Name the blood parasite species.
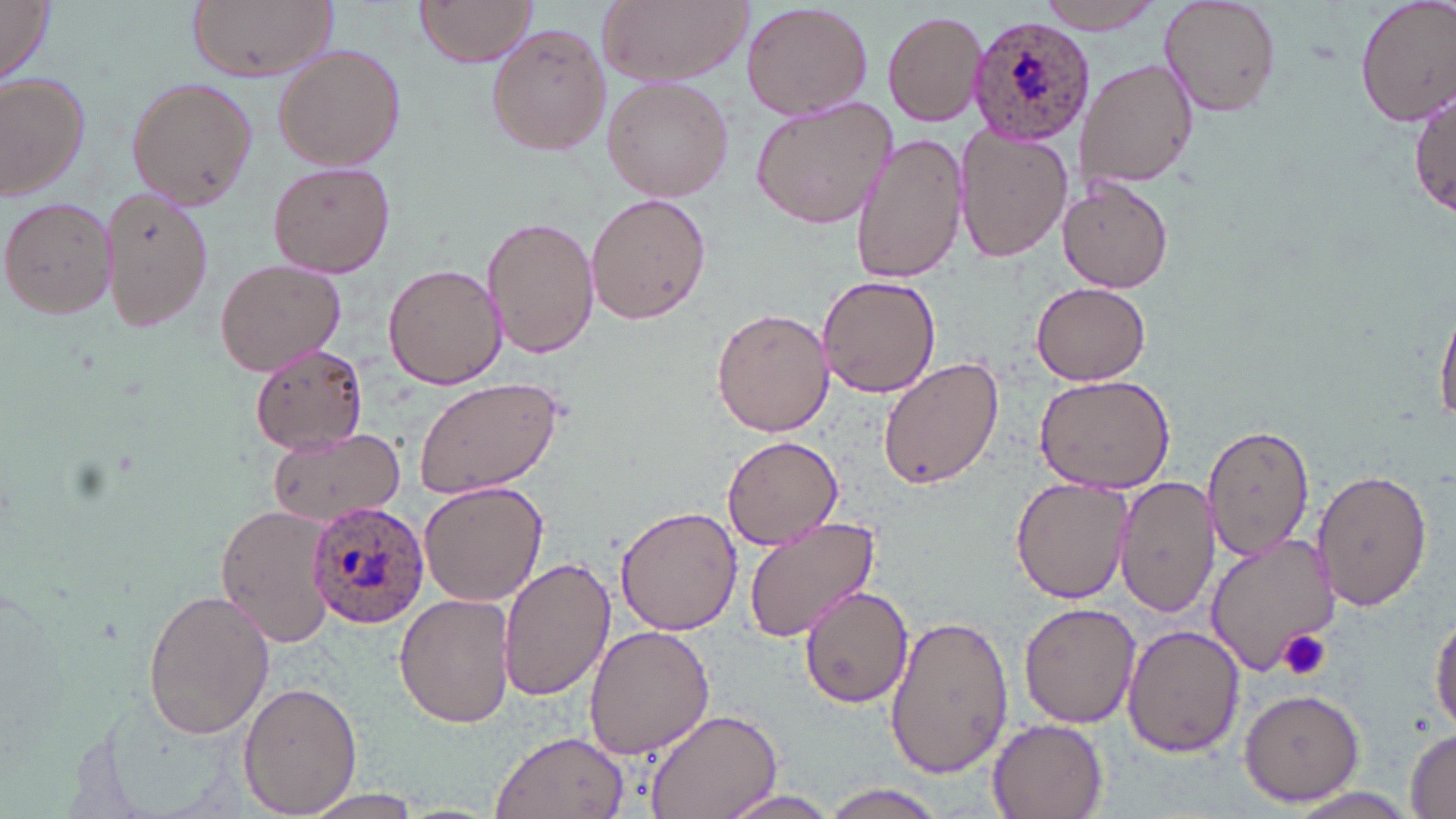

Plasmodium ovale.

Approximate bounding boxes as (x1, y1, x2, y2) in pixels. Uninfected red blood cell locations: (0, 0, 57, 85), (186, 0, 336, 80), (594, 0, 754, 86), (1042, 0, 1164, 33), (1159, 0, 1283, 118), (1354, 0, 1456, 128), (412, 1, 539, 68), (739, 1, 874, 122), (881, 9, 988, 125), (486, 24, 611, 156), (272, 43, 407, 173), (1077, 59, 1198, 188), (0, 73, 92, 199), (127, 76, 259, 209), (604, 76, 734, 202), (1412, 87, 1456, 220), (751, 98, 895, 230), (954, 124, 1072, 264), (849, 131, 967, 285), (268, 161, 396, 278), (1058, 177, 1174, 292), (101, 185, 216, 336), (585, 193, 711, 325), (0, 196, 116, 319), (483, 216, 599, 359), (217, 257, 348, 377), (384, 264, 506, 389), (816, 275, 941, 398), (1031, 281, 1151, 384), (1435, 304, 1456, 430), (711, 308, 835, 437), (248, 342, 367, 456), (877, 354, 1003, 490), (1035, 372, 1174, 493), (411, 376, 563, 500), (1203, 422, 1316, 563), (266, 427, 404, 526), (721, 434, 844, 549), (1313, 467, 1434, 612), (1115, 477, 1221, 621), (1011, 480, 1134, 603), (418, 481, 547, 605), (215, 504, 335, 648), (615, 505, 742, 636), (740, 514, 881, 643), (1205, 532, 1341, 675), (497, 558, 616, 700), (799, 586, 912, 709), (141, 588, 275, 742), (393, 593, 517, 728), (1019, 601, 1141, 727), (1430, 611, 1456, 736), (882, 612, 1014, 780), (582, 624, 717, 761), (1125, 624, 1246, 758), (235, 683, 362, 813), (1239, 688, 1366, 806), (644, 707, 783, 819), (988, 717, 1109, 819), (1404, 725, 1455, 819), (488, 729, 631, 818), (818, 784, 945, 819), (719, 789, 845, 819), (1283, 789, 1431, 819), (298, 790, 430, 818). Plasmodium ovale-infected red blood cell locations: (968, 15, 1097, 142), (307, 501, 431, 628). Platelet locations: (1278, 629, 1331, 682). May-Grünwald-Giemsa-stained preparation. Image is 1456×819 pixels. One field of a larger specimen. Thin blood film. Captured at 1000x magnification. Light microscopy.